Classify this cell by malaria status.
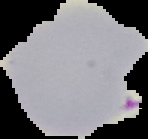

It is parasitized.

Summary:
  - Image size: 148×139 pixels
  - Image type: segmented cell region on a black background
  - Preparation: thin blood film